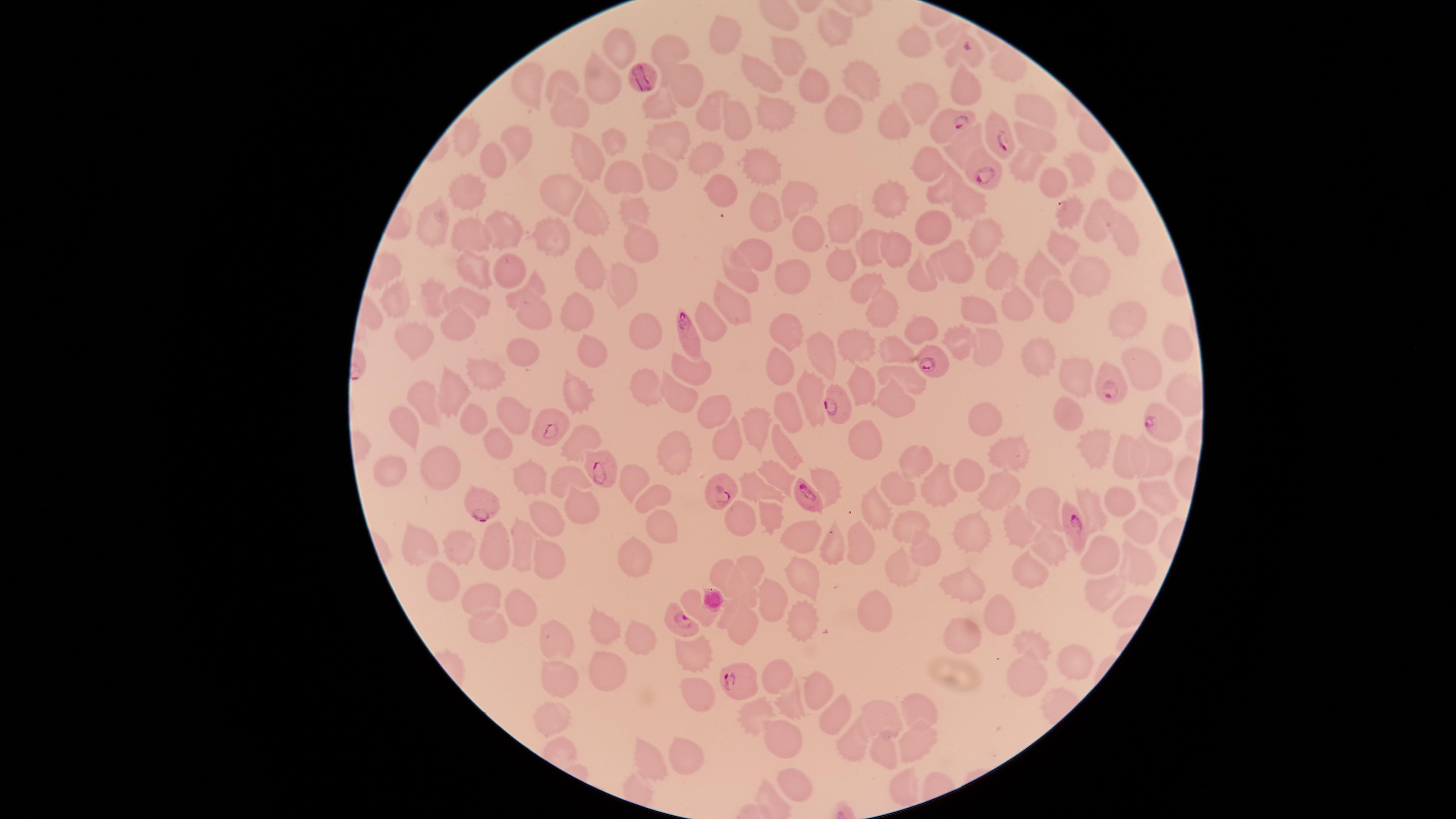
species: Plasmodium falciparum
field_of_view: single
preparation: thin blood film
uninfected_red_blood_cells: 'approximate marker points, in pixels from the top-left corner: (x=834, y=26), (x=725, y=33), (x=921, y=44), (x=666, y=46), (x=617, y=51), (x=790, y=55), (x=1007, y=66), (x=764, y=78), (x=685, y=79), (x=523, y=81), (x=568, y=81), (x=867, y=81), (x=967, y=81), (x=813, y=85), (x=597, y=86), (x=662, y=106), (x=710, y=106), (x=916, y=106), (x=1033, y=107), (x=773, y=112), (x=570, y=114), (x=847, y=115), (x=739, y=117), (x=894, y=120), (x=469, y=138), (x=671, y=138), (x=1039, y=138), (x=612, y=142), (x=517, y=144), (x=956, y=147), (x=706, y=152), (x=584, y=159), (x=1025, y=159), (x=1079, y=160), (x=494, y=161), (x=930, y=164), (x=761, y=165), (x=658, y=171), (x=622, y=178), (x=1119, y=179), (x=1054, y=181), (x=718, y=184), (x=558, y=188), (x=939, y=190), (x=469, y=191), (x=796, y=192), (x=891, y=199), (x=956, y=201), (x=763, y=208), (x=636, y=210), (x=1071, y=211), (x=592, y=216), (x=845, y=219), (x=434, y=220), (x=1098, y=222), (x=936, y=224), (x=507, y=230), (x=1126, y=230), (x=471, y=235), (x=554, y=235), (x=980, y=237), (x=806, y=238), (x=638, y=242), (x=1060, y=244), (x=871, y=247), (x=900, y=247), (x=758, y=253), (x=960, y=262), (x=843, y=263), (x=464, y=264), (x=508, y=269), (x=1043, y=269), (x=585, y=271), (x=1002, y=271), (x=1091, y=271), (x=793, y=273), (x=621, y=275), (x=923, y=279), (x=744, y=282), (x=855, y=285), (x=533, y=286), (x=435, y=298), (x=1061, y=301), (x=390, y=302), (x=473, y=302), (x=734, y=303), (x=876, y=304), (x=1015, y=304), (x=577, y=308), (x=977, y=311), (x=706, y=313), (x=535, y=314), (x=1121, y=316), (x=637, y=322), (x=454, y=327), (x=920, y=330), (x=785, y=336), (x=956, y=338), (x=1170, y=339), (x=415, y=340), (x=859, y=345), (x=892, y=347), (x=989, y=348), (x=523, y=354), (x=591, y=356), (x=820, y=356), (x=1037, y=356), (x=1141, y=361), (x=690, y=366), (x=779, y=367), (x=1071, y=371), (x=485, y=374), (x=905, y=375), (x=862, y=382), (x=646, y=388), (x=809, y=388), (x=453, y=389), (x=578, y=394), (x=425, y=395), (x=680, y=395), (x=894, y=398), (x=714, y=406), (x=787, y=410), (x=1072, y=410), (x=513, y=415), (x=470, y=420), (x=982, y=423), (x=759, y=425), (x=406, y=428), (x=580, y=440), (x=867, y=441), (x=495, y=442), (x=1092, y=442), (x=727, y=444), (x=1007, y=449), (x=785, y=451), (x=675, y=453), (x=916, y=459), (x=1118, y=460), (x=1158, y=460), (x=443, y=468), (x=390, y=469), (x=970, y=474), (x=778, y=476), (x=565, y=477), (x=626, y=477), (x=525, y=479), (x=942, y=484), (x=758, y=488), (x=896, y=489), (x=997, y=489), (x=1156, y=489), (x=651, y=492), (x=1121, y=500), (x=1047, y=505), (x=876, y=507), (x=578, y=508), (x=1090, y=508), (x=769, y=514), (x=740, y=519), (x=547, y=521), (x=1019, y=522), (x=972, y=523), (x=661, y=524), (x=905, y=524), (x=1139, y=525), (x=803, y=538), (x=522, y=541), (x=420, y=543), (x=829, y=543), (x=860, y=543), (x=492, y=544), (x=1045, y=545), (x=459, y=546), (x=928, y=548), (x=1104, y=552), (x=636, y=556), (x=547, y=557), (x=1129, y=562), (x=754, y=565), (x=719, y=569), (x=903, y=569), (x=1029, y=569), (x=803, y=577), (x=444, y=583), (x=973, y=585), (x=1098, y=590), (x=749, y=595), (x=771, y=595), (x=481, y=597), (x=521, y=605), (x=875, y=607), (x=728, y=610), (x=1001, y=610), (x=798, y=618), (x=743, y=625), (x=601, y=626), (x=489, y=631), (x=970, y=635), (x=637, y=636), (x=554, y=638), (x=1031, y=644), (x=694, y=657), (x=1078, y=657), (x=607, y=667), (x=1024, y=675), (x=774, y=677), (x=559, y=678), (x=812, y=685), (x=700, y=695), (x=789, y=702), (x=921, y=708), (x=755, y=709), (x=881, y=710), (x=546, y=713), (x=838, y=719), (x=779, y=740), (x=848, y=743), (x=921, y=744), (x=884, y=751), (x=682, y=754), (x=648, y=762), (x=906, y=785), (x=795, y=788)'
parasitized_red_blood_cells: 'approximate marker points, in pixels from the top-left corner: (x=969, y=50), (x=951, y=126), (x=996, y=137), (x=985, y=175), (x=691, y=335), (x=934, y=361), (x=1106, y=381), (x=838, y=403), (x=1156, y=422), (x=554, y=426), (x=600, y=469), (x=719, y=487), (x=804, y=491), (x=481, y=502), (x=1074, y=526), (x=679, y=621), (x=734, y=680)'
stain: Giemsa
visible_region: circular
capture: smartphone photograph through the microscope eyepiece
presence: malaria parasites identified
image_size: 1456×819 pixels